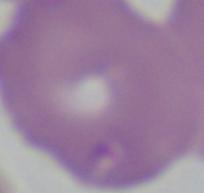
identification: Babesia
magnification: 1000x
modality: photomicrograph